Classify this cell by malaria status.
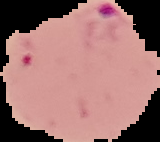

It is parasitized.

Summary:
  - Preparation: thin blood smear
  - Image size: 160×142 pixels
  - Image type: cell region segmented out of the field of view; surrounding area masked to black